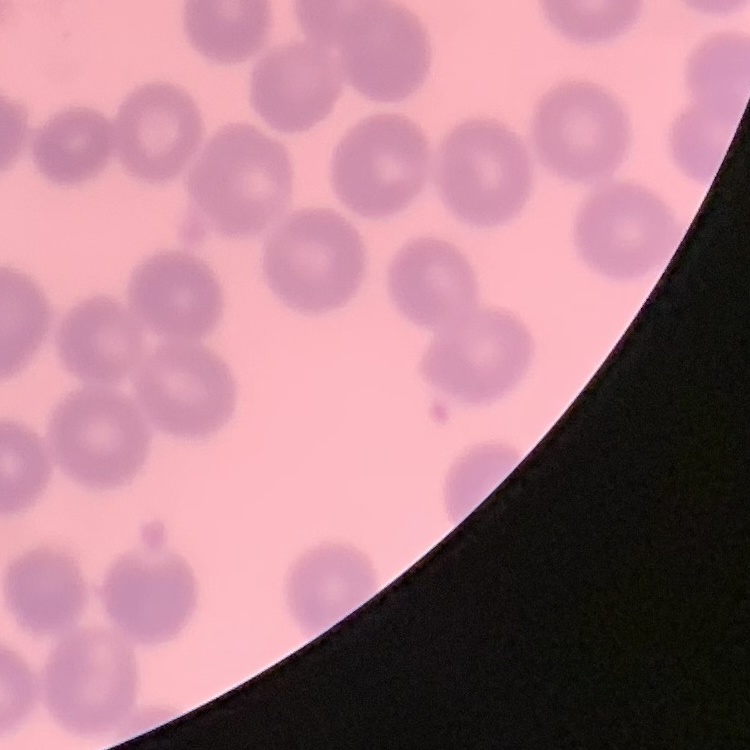
erythrocyte morphology = no rouleaux formation
image type = square crop of a larger photomicrograph
stain = Field's or Giemsa
preparation = thin blood smear